Name the parasite shown.
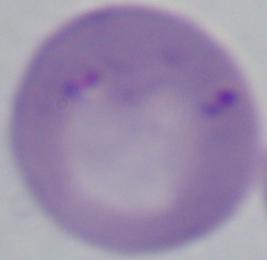
Babesia.

Micrograph. 1000x magnification.